Locate and identify every blood parasite.
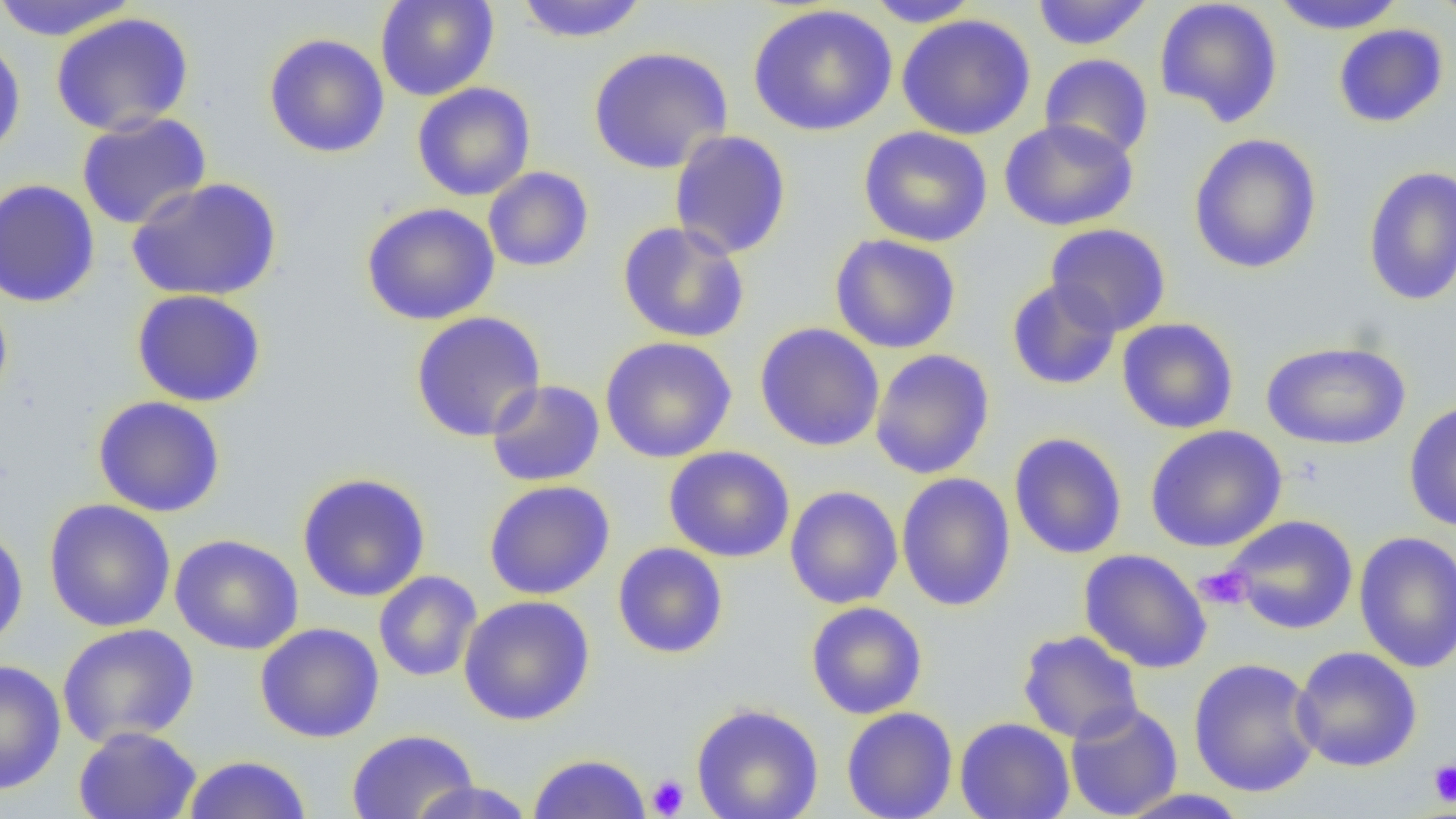
No blood parasites observed.

Summary:
  - Coordinate format: approximate bounding boxes as (x1, y1, x2, y2) in pixels
  - Uninfected red blood cell locations: (0, 0, 140, 41), (375, 0, 499, 101), (514, 0, 650, 43), (863, 0, 983, 27), (1031, 0, 1154, 50), (1154, 0, 1284, 128), (1268, 0, 1407, 34), (1430, 0, 1456, 28), (747, 4, 898, 137), (49, 12, 194, 137), (896, 14, 1036, 140), (1333, 24, 1449, 128), (263, 33, 390, 158), (0, 36, 27, 164), (588, 45, 733, 174), (1039, 53, 1154, 161), (412, 82, 536, 201), (76, 112, 212, 229), (999, 118, 1139, 232), (858, 126, 993, 248), (669, 130, 792, 260), (1188, 133, 1323, 275), (1362, 165, 1456, 306), (483, 166, 594, 272), (0, 178, 101, 308), (125, 178, 282, 301), (360, 202, 500, 326), (616, 221, 751, 344), (1045, 223, 1171, 336), (829, 233, 961, 354), (1005, 278, 1122, 391), (131, 289, 267, 407), (0, 291, 13, 411), (409, 311, 546, 442), (1116, 318, 1239, 434), (754, 322, 885, 452), (599, 336, 737, 463), (1260, 341, 1411, 450), (869, 349, 995, 479), (486, 380, 605, 487), (92, 396, 226, 517), (1403, 399, 1456, 533), (1145, 425, 1287, 553), (1009, 432, 1128, 560), (663, 446, 795, 562), (297, 471, 431, 602), (896, 472, 1016, 612), (483, 480, 616, 600), (785, 485, 903, 610), (44, 498, 176, 632), (1221, 514, 1359, 635), (0, 524, 29, 652), (1354, 531, 1456, 673), (169, 534, 304, 655), (612, 542, 729, 659), (1078, 548, 1213, 673), (373, 570, 482, 682), (457, 595, 595, 726), (805, 601, 928, 719), (254, 622, 384, 743), (56, 623, 200, 748), (1017, 630, 1144, 744), (1290, 646, 1423, 771), (1187, 657, 1322, 798), (1, 659, 66, 795), (1064, 701, 1183, 818), (690, 702, 824, 819), (841, 707, 958, 819), (954, 717, 1075, 819), (73, 726, 202, 819), (346, 728, 479, 819), (527, 752, 652, 818), (182, 754, 312, 819), (406, 780, 538, 818), (1113, 788, 1252, 819)
  - Platelet locations: (1194, 565, 1253, 611), (1427, 759, 1456, 808), (647, 774, 689, 817)
  - Slide-level diagnosis: negative for blood parasites
  - Modality: optical microscopy
  - Field of view: single
  - Image size: 1456×819 pixels
  - Preparation: thin blood film
  - Magnification: 1000x